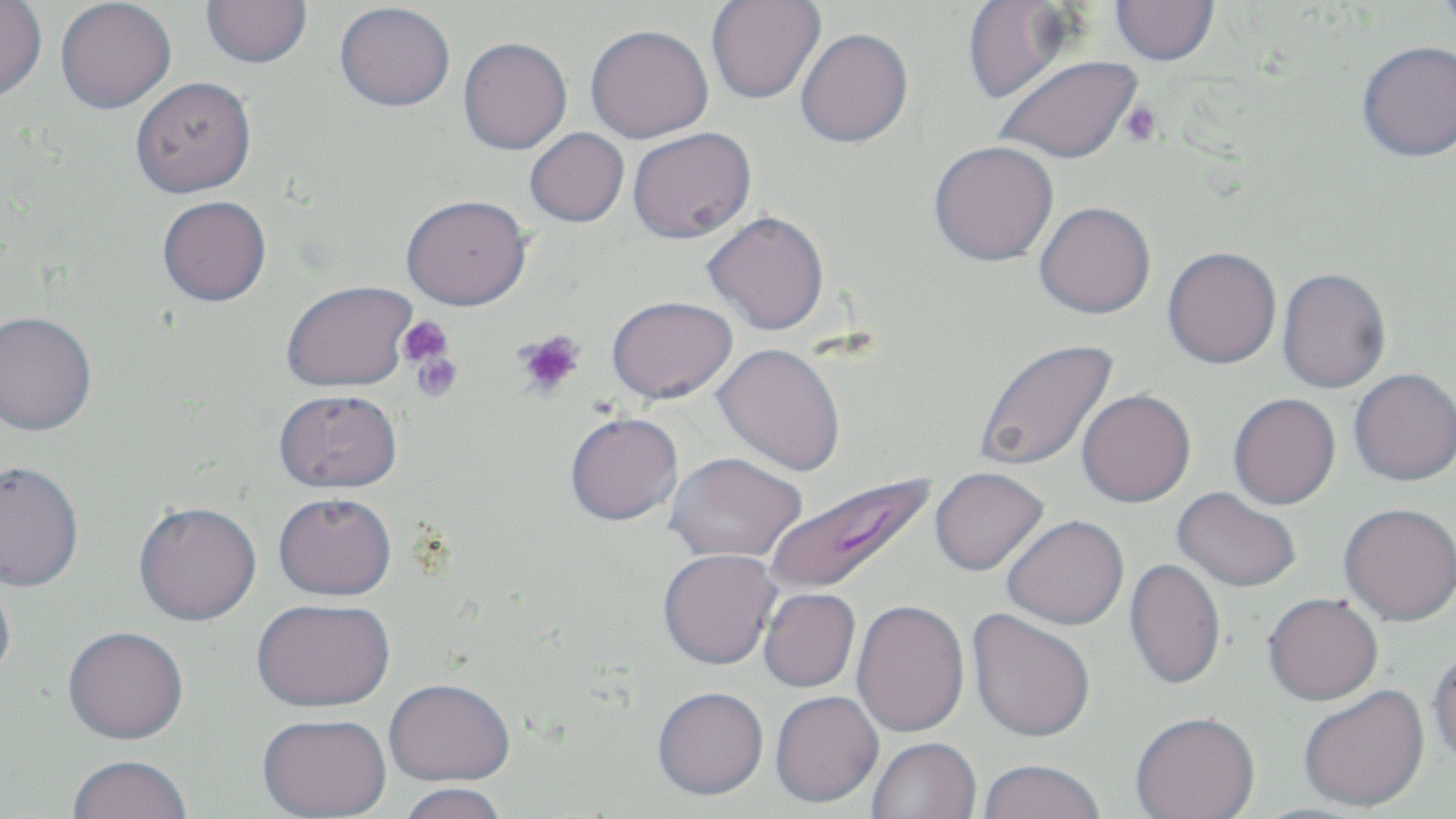
Plasmodium falciparum-infected red blood cell locations = approximate bounding boxes as named x1/y1/x2/y2 corners in pixels: (x1=761, y1=470, x2=938, y2=597)
slide-level diagnosis = Plasmodium falciparum
magnification = 1000x
preparation = thin blood smear
platelet locations = approximate bounding boxes as named x1/y1/x2/y2 corners in pixels: (x1=1120, y1=102, x2=1163, y2=147), (x1=398, y1=317, x2=454, y2=368), (x1=514, y1=330, x2=586, y2=398), (x1=410, y1=349, x2=462, y2=402)
modality = light microscopy
image size = 1456×819 pixels
uninfected red blood cell locations = approximate bounding boxes as named x1/y1/x2/y2 corners in pixels: (x1=55, y1=0, x2=176, y2=113), (x1=202, y1=0, x2=312, y2=68), (x1=1435, y1=0, x2=1456, y2=36), (x1=0, y1=1, x2=47, y2=101), (x1=706, y1=1, x2=825, y2=104), (x1=959, y1=1, x2=1081, y2=105), (x1=1109, y1=1, x2=1219, y2=66), (x1=335, y1=2, x2=455, y2=111), (x1=585, y1=24, x2=713, y2=143), (x1=795, y1=28, x2=913, y2=148), (x1=458, y1=37, x2=572, y2=154), (x1=1357, y1=40, x2=1456, y2=162), (x1=994, y1=55, x2=1143, y2=164), (x1=130, y1=76, x2=256, y2=197), (x1=525, y1=127, x2=629, y2=227), (x1=627, y1=127, x2=756, y2=243), (x1=929, y1=140, x2=1059, y2=266), (x1=401, y1=194, x2=531, y2=310), (x1=157, y1=195, x2=271, y2=305), (x1=1034, y1=201, x2=1156, y2=318), (x1=703, y1=211, x2=829, y2=335), (x1=1163, y1=246, x2=1282, y2=368), (x1=1276, y1=267, x2=1391, y2=393), (x1=281, y1=280, x2=416, y2=392), (x1=607, y1=295, x2=737, y2=402), (x1=0, y1=310, x2=97, y2=436), (x1=974, y1=338, x2=1119, y2=473), (x1=713, y1=343, x2=846, y2=477), (x1=1348, y1=368, x2=1456, y2=486), (x1=274, y1=389, x2=403, y2=493), (x1=1076, y1=389, x2=1196, y2=507), (x1=1228, y1=393, x2=1341, y2=509), (x1=565, y1=411, x2=684, y2=526), (x1=666, y1=452, x2=805, y2=562), (x1=0, y1=461, x2=85, y2=592), (x1=929, y1=466, x2=1049, y2=576), (x1=1172, y1=486, x2=1301, y2=592), (x1=274, y1=491, x2=397, y2=600), (x1=133, y1=501, x2=262, y2=625), (x1=1339, y1=502, x2=1456, y2=625), (x1=1002, y1=514, x2=1129, y2=630), (x1=658, y1=548, x2=781, y2=669), (x1=1124, y1=558, x2=1226, y2=690), (x1=0, y1=574, x2=16, y2=690), (x1=758, y1=587, x2=860, y2=692), (x1=1263, y1=592, x2=1383, y2=704), (x1=251, y1=598, x2=395, y2=711), (x1=851, y1=599, x2=970, y2=737), (x1=967, y1=608, x2=1096, y2=742), (x1=63, y1=626, x2=189, y2=746), (x1=1428, y1=644, x2=1456, y2=765), (x1=384, y1=677, x2=515, y2=787), (x1=1298, y1=684, x2=1430, y2=812), (x1=653, y1=686, x2=769, y2=799), (x1=770, y1=691, x2=883, y2=808), (x1=1130, y1=711, x2=1260, y2=819), (x1=257, y1=714, x2=392, y2=818), (x1=867, y1=737, x2=981, y2=819), (x1=67, y1=757, x2=192, y2=819), (x1=977, y1=759, x2=1106, y2=819), (x1=395, y1=782, x2=509, y2=819)
stain = May-Grünwald-Giemsa
field of view = single